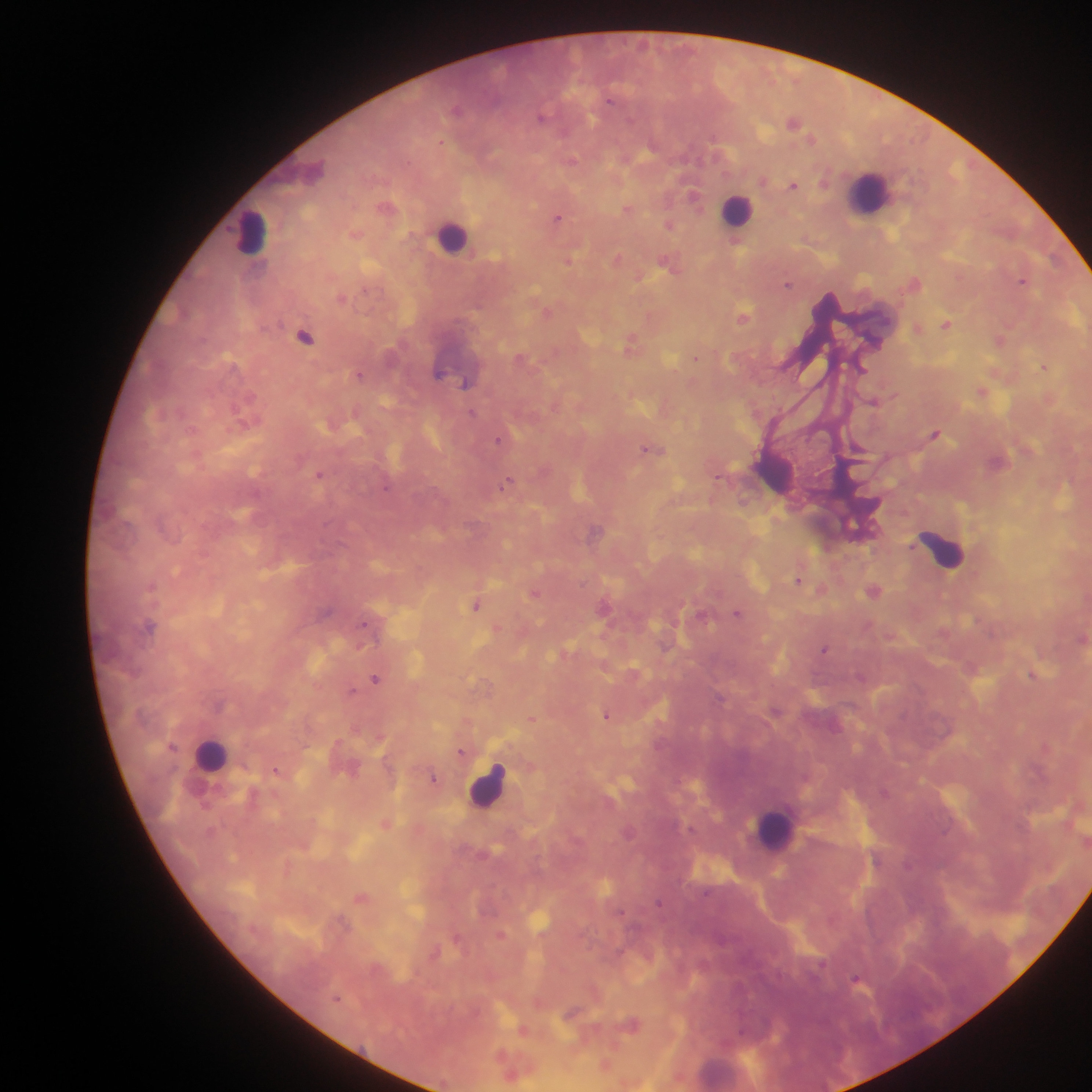

image size = 1092×1092 pixels
field of view = single
country = Ghana
preparation = thick blood smear
leukocyte locations = approximate centers as [x, y] in pixels: [870, 194], [737, 210], [252, 233], [453, 237], [774, 470], [943, 549], [211, 755], [488, 785], [775, 829]
capture = mobile-phone photograph through a microscope
malaria parasite locations = approximate centers as [x, y] in pixels: [457, 109], [542, 116], [793, 121], [572, 160], [793, 185], [694, 195], [387, 206], [628, 208], [557, 218], [669, 223], [356, 233], [735, 240], [619, 258], [569, 260], [669, 263], [1023, 280], [915, 281], [788, 284], [343, 297], [548, 310], [744, 317], [946, 323], [917, 328], [304, 335], [1001, 338], [631, 344], [696, 357], [523, 359], [1044, 365], [862, 368], [359, 374], [467, 382], [982, 391], [875, 401], [472, 413], [247, 419], [936, 433], [500, 439], [651, 449], [320, 473], [509, 481], [386, 487], [596, 530], [799, 579], [822, 589], [873, 590], [535, 592], [476, 604], [605, 606], [738, 613], [150, 626], [498, 629], [1082, 637], [824, 649], [566, 652], [1034, 674], [376, 678], [351, 691], [607, 714], [532, 718], [1046, 746], [172, 747], [462, 752], [277, 769], [434, 778], [385, 823], [361, 898], [660, 902], [501, 934], [458, 938], [435, 952], [858, 980], [572, 1012], [631, 1024], [523, 1030], [605, 1064], [512, 1072]